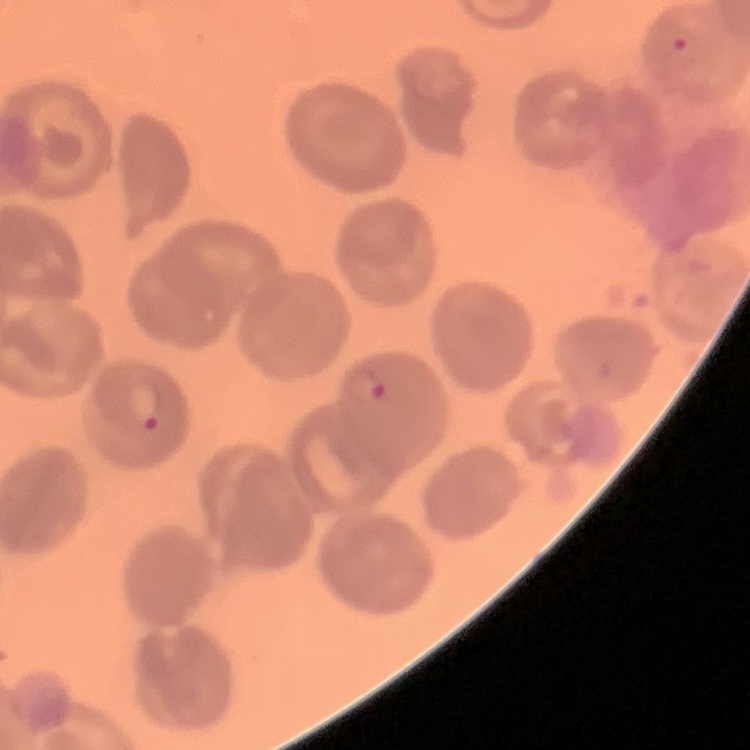
Summary:
  - Red blood cell morphology: no rouleaux formation
  - Stain: Field's or Giemsa
  - Preparation: thin peripheral smear
  - Image type: square crop of a larger photomicrograph